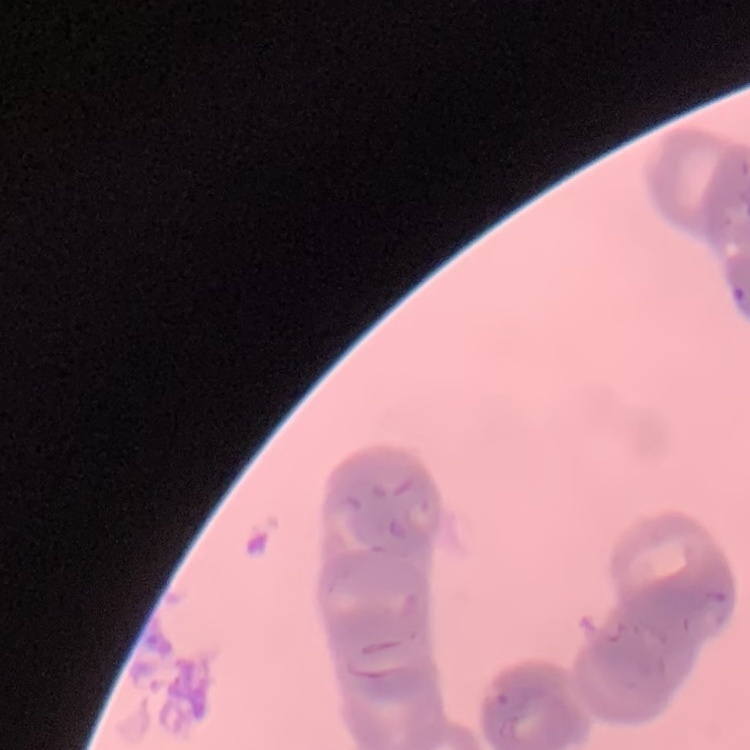

Summary:
  - Red blood cell morphology: rouleaux formation
  - Image type: square crop of a larger photomicrograph
  - Preparation: thin blood smear
  - Stain: Field's or Giemsa